Report the malaria status of this cell.
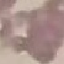
It is uninfected.

capture: smartphone camera at the microscope eyepiece
preparation: thin blood film
image_type: automatically extracted cell patch, resized to 64 × 64 pixels
stain: Giemsa